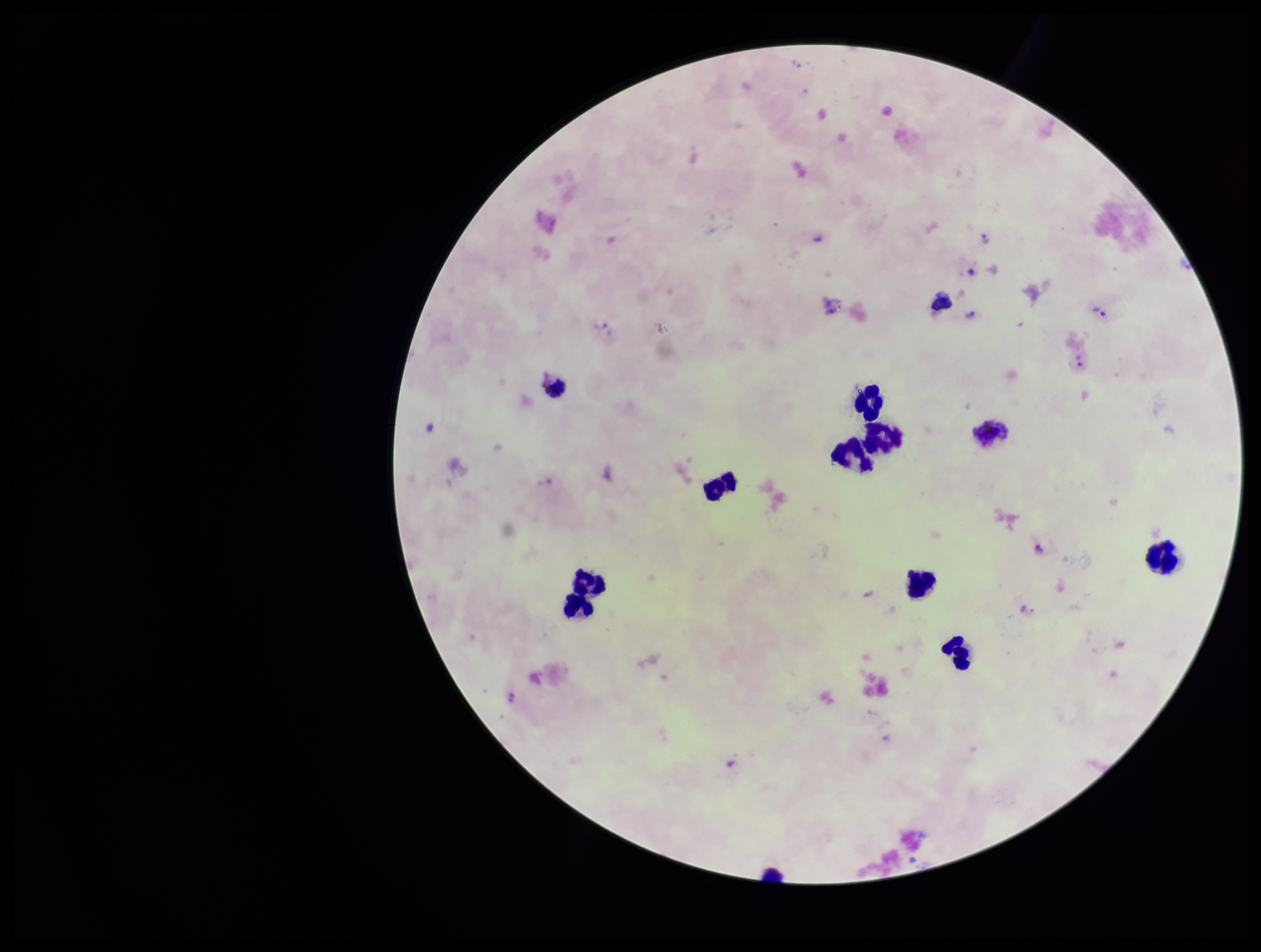

Summary:
  - Stain: Giemsa
  - Species reported for this patient: Plasmodium vivax
  - Preparation: thick
  - Leukocyte count: 11
  - Field of view: one from this slide
  - Capture: smartphone photograph through the microscope eyepiece
  - Image size: 1261×952 pixels
  - Patient malaria status: infected
  - Parasite count: 8
  - Plasmodium parasites: identified